Classify this cell by malaria status.
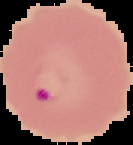

It is parasitized.

image size = 133×145 pixels
image type = cell region segmented out of the field of view; surrounding area masked to black
preparation = thin blood smear